Name the parasite shown.
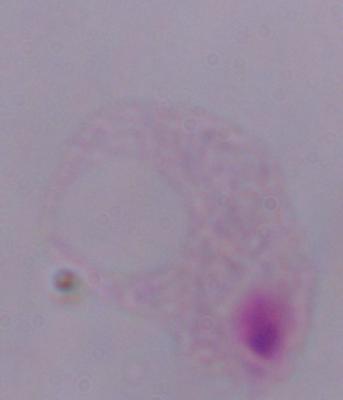
A trichomonad.

Summary:
  - Modality: photomicrograph
  - Magnification: 1000x